Locate every blood parasite and identify its species.
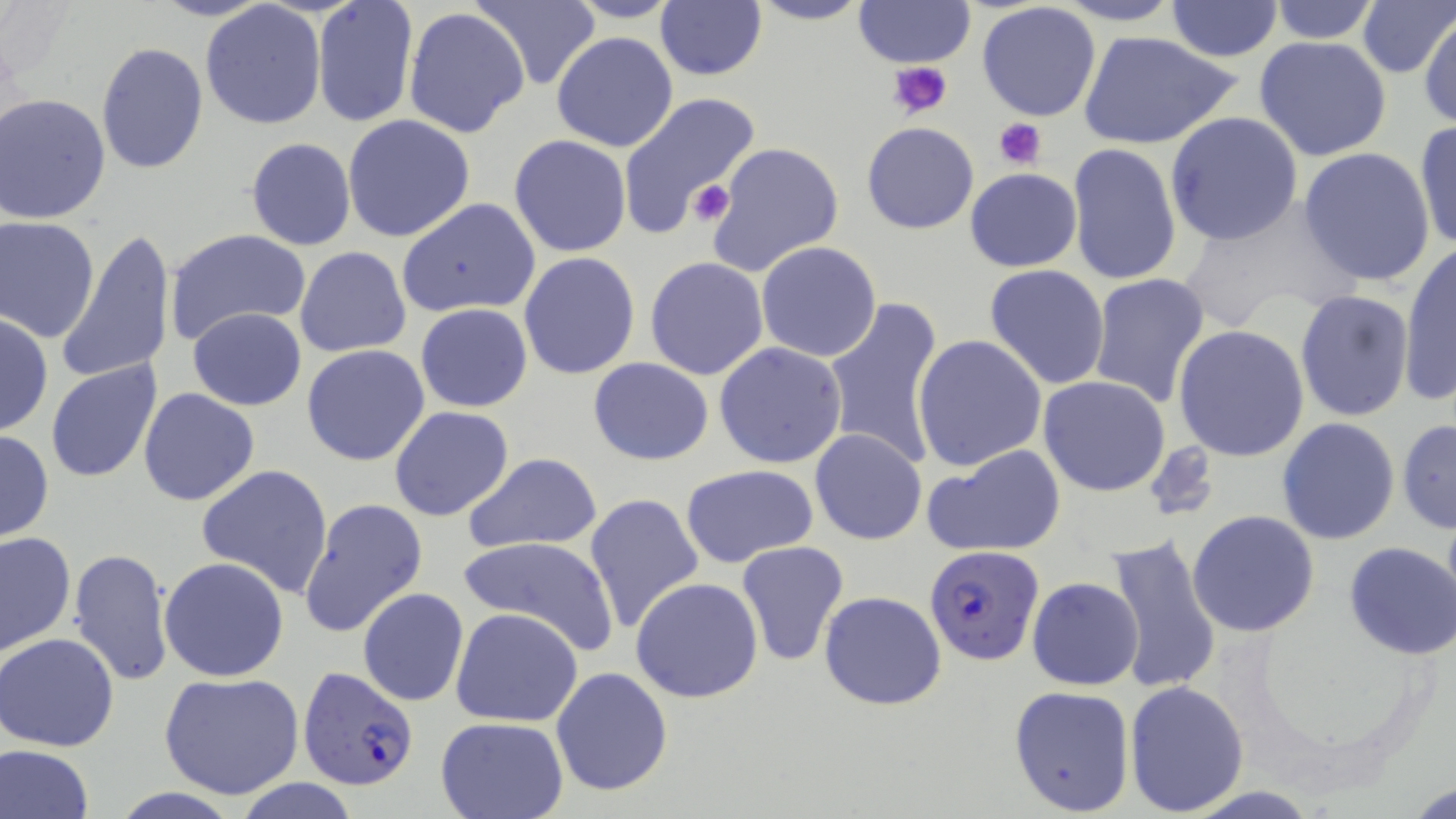

Approximate bounding boxes as named x1/y1/x2/y2 corners in pixels.
Plasmodium falciparum-infected red blood cells: (x1=925, y1=544, x2=1045, y2=668), (x1=294, y1=660, x2=417, y2=787).
No Plasmodium ovale, Plasmodium malariae, Plasmodium vivax, Babesia divergens, or Trypanosoma brucei observed.

Summary:
  - Uninfected red blood cell locations: (x1=149, y1=0, x2=276, y2=22), (x1=311, y1=0, x2=419, y2=128), (x1=467, y1=0, x2=603, y2=92), (x1=565, y1=0, x2=686, y2=24), (x1=749, y1=0, x2=872, y2=26), (x1=852, y1=0, x2=976, y2=67), (x1=1265, y1=0, x2=1384, y2=45), (x1=1356, y1=0, x2=1455, y2=79), (x1=976, y1=1, x2=1102, y2=123), (x1=1057, y1=1, x2=1189, y2=27), (x1=654, y1=2, x2=767, y2=81), (x1=1166, y1=2, x2=1282, y2=61), (x1=199, y1=3, x2=327, y2=132), (x1=403, y1=7, x2=531, y2=141), (x1=1418, y1=14, x2=1455, y2=128), (x1=1077, y1=30, x2=1242, y2=150), (x1=551, y1=32, x2=679, y2=153), (x1=1253, y1=36, x2=1393, y2=162), (x1=95, y1=42, x2=209, y2=174), (x1=618, y1=91, x2=763, y2=238), (x1=1, y1=94, x2=111, y2=224), (x1=1165, y1=112, x2=1304, y2=248), (x1=342, y1=115, x2=475, y2=242), (x1=1412, y1=119, x2=1456, y2=255), (x1=861, y1=122, x2=980, y2=233), (x1=509, y1=134, x2=632, y2=258), (x1=246, y1=137, x2=357, y2=252), (x1=704, y1=141, x2=845, y2=278), (x1=1066, y1=142, x2=1181, y2=290), (x1=1297, y1=147, x2=1438, y2=288), (x1=964, y1=168, x2=1082, y2=273), (x1=396, y1=198, x2=541, y2=319), (x1=1173, y1=209, x2=1348, y2=333), (x1=0, y1=215, x2=100, y2=340), (x1=163, y1=228, x2=311, y2=345), (x1=55, y1=229, x2=176, y2=386), (x1=755, y1=240, x2=882, y2=362), (x1=1399, y1=244, x2=1456, y2=406), (x1=296, y1=247, x2=411, y2=358), (x1=517, y1=250, x2=640, y2=380), (x1=742, y1=254, x2=910, y2=436), (x1=644, y1=257, x2=769, y2=381), (x1=984, y1=264, x2=1110, y2=391), (x1=1088, y1=272, x2=1211, y2=407), (x1=1294, y1=289, x2=1416, y2=425), (x1=823, y1=298, x2=947, y2=469), (x1=415, y1=303, x2=532, y2=413), (x1=186, y1=307, x2=307, y2=411), (x1=0, y1=312, x2=51, y2=438), (x1=1173, y1=325, x2=1310, y2=463), (x1=913, y1=335, x2=1048, y2=472), (x1=714, y1=341, x2=848, y2=467), (x1=301, y1=344, x2=431, y2=466), (x1=45, y1=358, x2=163, y2=485), (x1=588, y1=358, x2=714, y2=466), (x1=1037, y1=375, x2=1170, y2=496), (x1=139, y1=387, x2=259, y2=506), (x1=389, y1=405, x2=514, y2=523), (x1=1277, y1=417, x2=1400, y2=545), (x1=1397, y1=418, x2=1455, y2=534), (x1=809, y1=428, x2=927, y2=545), (x1=0, y1=430, x2=53, y2=544), (x1=922, y1=444, x2=1066, y2=557), (x1=461, y1=453, x2=604, y2=554), (x1=195, y1=464, x2=334, y2=597), (x1=679, y1=465, x2=820, y2=568), (x1=583, y1=492, x2=705, y2=633), (x1=298, y1=496, x2=429, y2=639), (x1=1187, y1=510, x2=1320, y2=637), (x1=1, y1=531, x2=75, y2=658), (x1=456, y1=534, x2=619, y2=654), (x1=1101, y1=534, x2=1224, y2=700), (x1=735, y1=541, x2=849, y2=667), (x1=1343, y1=542, x2=1455, y2=661), (x1=66, y1=548, x2=174, y2=689), (x1=158, y1=556, x2=291, y2=683), (x1=630, y1=577, x2=764, y2=704), (x1=1027, y1=577, x2=1143, y2=690), (x1=358, y1=587, x2=469, y2=707), (x1=818, y1=591, x2=947, y2=710), (x1=450, y1=606, x2=584, y2=727), (x1=497, y1=618, x2=664, y2=763), (x1=1, y1=632, x2=120, y2=752), (x1=551, y1=666, x2=672, y2=796), (x1=158, y1=671, x2=304, y2=799), (x1=1124, y1=680, x2=1251, y2=815), (x1=1008, y1=685, x2=1135, y2=815), (x1=434, y1=716, x2=568, y2=819), (x1=1, y1=744, x2=96, y2=819), (x1=236, y1=780, x2=363, y2=818), (x1=1408, y1=780, x2=1455, y2=818)
  - Platelet locations: (x1=888, y1=59, x2=955, y2=120), (x1=993, y1=117, x2=1047, y2=170), (x1=690, y1=182, x2=736, y2=227)
  - Slide-level diagnosis: Plasmodium falciparum
  - Image size: 1456×819 pixels
  - Magnification: 1000x
  - Modality: light microscopy
  - Stain: May-Grünwald-Giemsa
  - Preparation: thin blood film
  - Field of view: one of a larger specimen